Classify this cell by malaria status.
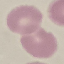
Uninfected.

image type = automatically extracted cell patch, resized to 64 × 64 pixels
stain = Giemsa
capture = smartphone through the microscope eyepiece
preparation = thin blood film